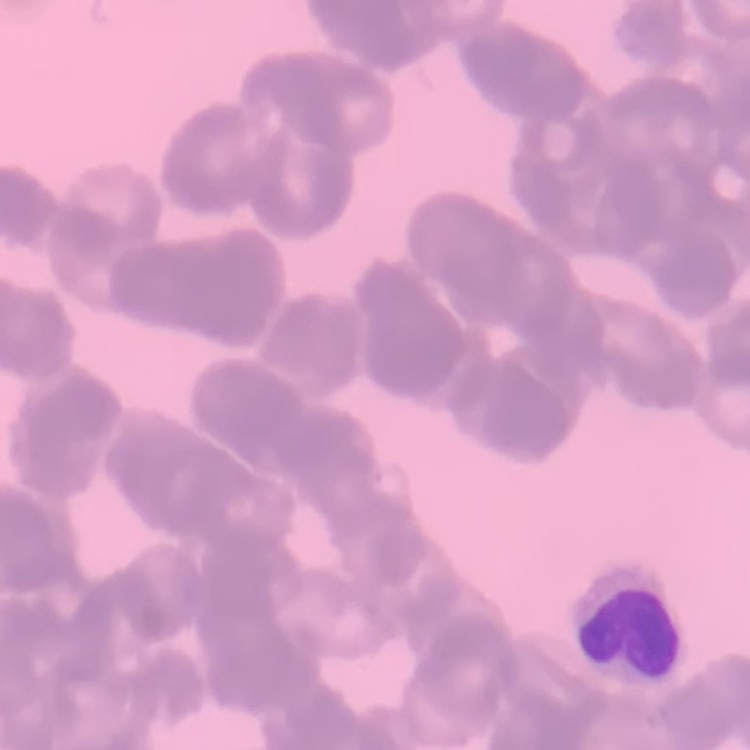
Summary:
  - Erythrocyte morphology: rouleaux formation
  - Stain: Field's or Giemsa
  - Image type: square crop of a larger photomicrograph
  - Preparation: thin blood film